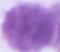

Captured at 1000x magnification. Photomicrograph. A red blood cell is shown.